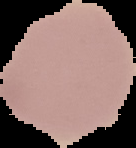
Summary:
  - Preparation: thin blood film
  - Malaria status: uninfected
  - Image size: 136×148 pixels
  - Image type: segmented cell region with the area outside set to black